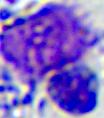

modality = photomicrograph
identification = leukocyte
magnification = 400x